Report the malaria status of this cell.
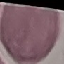
Uninfected.

Summary:
  - Image type: automatically extracted cell patch, resized to 64 × 64 pixels
  - Capture: smartphone through the microscope eyepiece
  - Preparation: thin smear
  - Stain: Giemsa